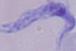
A trypanosome is shown. Photomicrograph. Captured at 1000x magnification.